Give the extent of all Plasmodium falciparum-infected red blood cells.
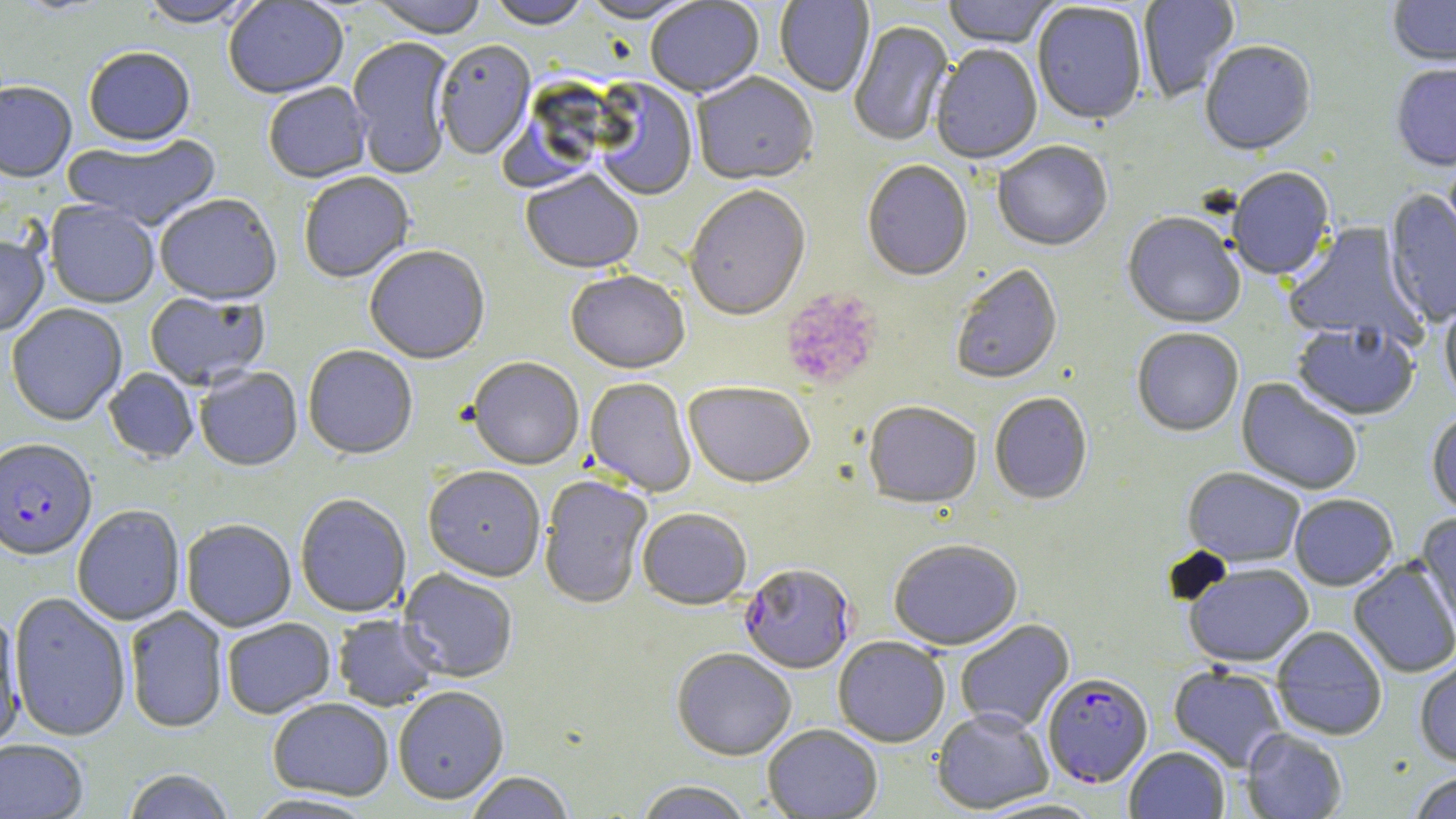
Approximate bounding boxes as (x1, y1, x2, y2) in pixels.
Plasmodium falciparum-infected red blood cells: (0, 441, 97, 563), (738, 564, 856, 675), (1042, 673, 1153, 788).

Platelet locations: (780, 289, 883, 391). Uninfected red blood cell locations: (13, 0, 114, 17), (140, 0, 260, 31), (224, 0, 349, 101), (368, 0, 488, 41), (488, 0, 590, 31), (578, 0, 701, 25), (645, 0, 765, 100), (775, 0, 874, 98), (942, 0, 1058, 50), (1138, 0, 1240, 103), (1387, 0, 1456, 70), (1032, 4, 1147, 128), (848, 21, 955, 148), (348, 38, 455, 179), (435, 42, 536, 161), (1200, 42, 1317, 159), (931, 47, 1042, 166), (84, 50, 195, 150), (1391, 64, 1456, 174), (691, 74, 818, 188), (593, 81, 698, 202), (0, 83, 77, 185), (263, 84, 372, 185), (62, 134, 221, 233), (993, 143, 1113, 253), (862, 162, 973, 283), (1227, 168, 1336, 283), (521, 172, 644, 277), (299, 173, 415, 285), (685, 187, 812, 324), (1384, 189, 1456, 328), (155, 196, 282, 308), (45, 202, 160, 309), (1122, 213, 1245, 330), (1283, 222, 1425, 347), (0, 235, 50, 338), (364, 247, 490, 367), (951, 266, 1063, 386), (566, 272, 690, 376), (144, 292, 270, 391), (1439, 295, 1456, 413), (6, 305, 127, 427), (1290, 323, 1420, 422), (1132, 329, 1244, 438), (303, 347, 418, 461), (467, 359, 584, 471), (195, 368, 303, 473), (104, 369, 199, 464), (1236, 378, 1363, 495), (584, 379, 696, 498), (683, 384, 814, 490), (989, 393, 1093, 505), (864, 403, 981, 510), (1426, 411, 1456, 520), (423, 468, 545, 583), (1182, 468, 1306, 568), (538, 476, 652, 610), (1289, 494, 1398, 591), (295, 495, 411, 618), (72, 506, 185, 626), (637, 510, 752, 611), (1416, 513, 1456, 636), (182, 520, 297, 633), (889, 541, 1023, 651), (1348, 558, 1456, 678), (1183, 563, 1315, 669), (398, 569, 518, 683), (9, 593, 131, 742), (125, 607, 228, 735), (0, 613, 25, 750), (333, 615, 442, 711), (222, 618, 336, 720), (955, 619, 1074, 733), (1271, 626, 1387, 741), (833, 638, 949, 747), (671, 649, 796, 761), (1414, 654, 1456, 767), (1169, 665, 1288, 772), (393, 688, 509, 806), (268, 699, 394, 801), (932, 709, 1053, 814), (763, 725, 883, 818), (1241, 728, 1347, 818), (0, 740, 89, 818), (1124, 746, 1229, 819), (121, 769, 236, 819), (1407, 770, 1456, 819), (464, 772, 575, 819), (635, 781, 752, 819), (243, 794, 379, 818). Slide-level diagnosis: Plasmodium falciparum. One field of a larger specimen. Image is 1456×819 pixels. Captured at 1000x magnification. Optical microscopy. May-Grünwald-Giemsa-stained preparation. Thin blood smear.